Outline each blood parasite and name the species.
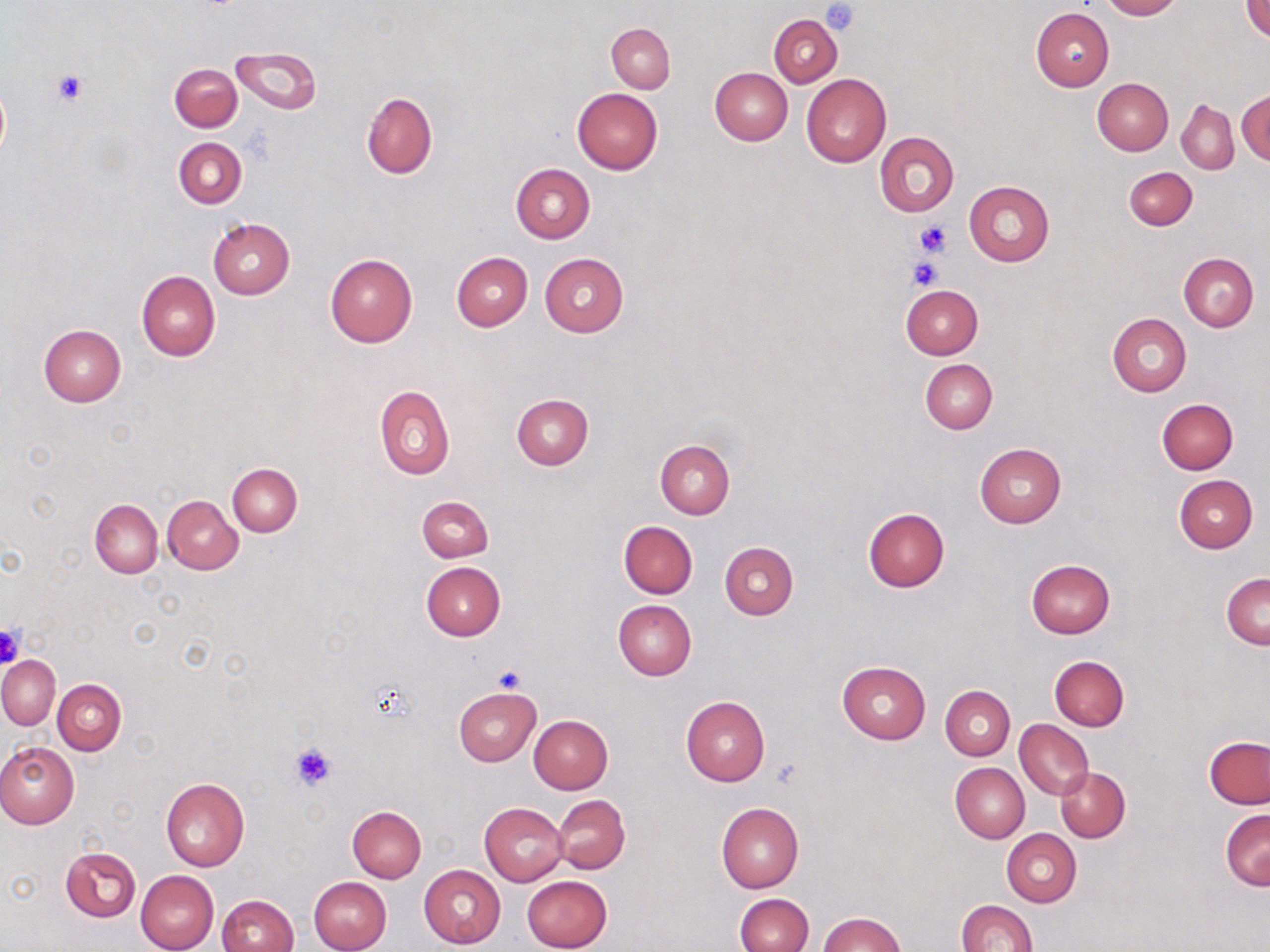
No blood parasites observed.

Approximate bounding boxes as (x1,y1)-(x2,y2) corner pairs in pixels. Uninfected red blood cell locations: (1100,0)-(1180,20), (1242,0)-(1270,41), (1031,7)-(1115,91), (769,15)-(842,87), (606,22)-(675,93), (230,45)-(322,115), (170,63)-(241,132), (709,68)-(793,145), (802,74)-(890,167), (1091,78)-(1173,155), (573,87)-(663,174), (1236,89)-(1270,165), (361,93)-(437,178), (1176,100)-(1238,174), (874,132)-(959,216), (174,137)-(246,208), (510,163)-(595,243), (1124,167)-(1197,230), (964,181)-(1055,266), (207,218)-(294,299), (451,251)-(533,331), (324,253)-(416,348), (540,253)-(628,338), (1179,253)-(1257,331), (137,270)-(220,360), (900,284)-(983,360), (1108,312)-(1191,397), (39,323)-(126,406), (920,358)-(997,434), (374,385)-(454,480), (511,395)-(593,469), (1156,398)-(1238,475), (655,440)-(734,519), (975,443)-(1065,528), (227,463)-(302,536), (1174,474)-(1258,553), (161,496)-(242,575), (417,496)-(493,562), (90,498)-(163,577), (862,508)-(950,592), (619,521)-(697,599), (719,542)-(798,621), (1026,559)-(1115,638), (421,562)-(504,640), (1222,572)-(1269,650), (613,599)-(696,680), (0,656)-(60,730), (1050,656)-(1129,730), (838,661)-(930,744), (53,678)-(126,755), (941,685)-(1015,760), (454,687)-(541,766), (681,695)-(770,786), (529,716)-(612,794), (1015,721)-(1092,799), (1204,735)-(1270,809), (0,743)-(78,829), (950,762)-(1030,843), (1055,767)-(1130,842), (161,778)-(249,871), (553,795)-(630,873), (480,803)-(567,886), (717,803)-(803,892), (347,805)-(426,883), (1220,810)-(1270,891), (1002,829)-(1082,906), (60,847)-(140,921), (418,865)-(505,947), (136,870)-(219,952), (521,875)-(613,952), (309,877)-(392,952), (735,893)-(812,952), (218,894)-(298,952), (955,900)-(1037,952), (818,913)-(906,952). Platelet locations: (820,1)-(862,36), (52,71)-(88,106), (915,220)-(952,256), (907,256)-(942,290), (0,624)-(24,670), (491,667)-(525,694), (290,743)-(338,791), (769,760)-(800,787). Slide-level diagnosis: negative for blood parasites. One field of a larger specimen. 1000x magnification. Thin blood smear. Image is 1270×952 pixels. May-Grünwald-Giemsa stain. Optical microscopy.